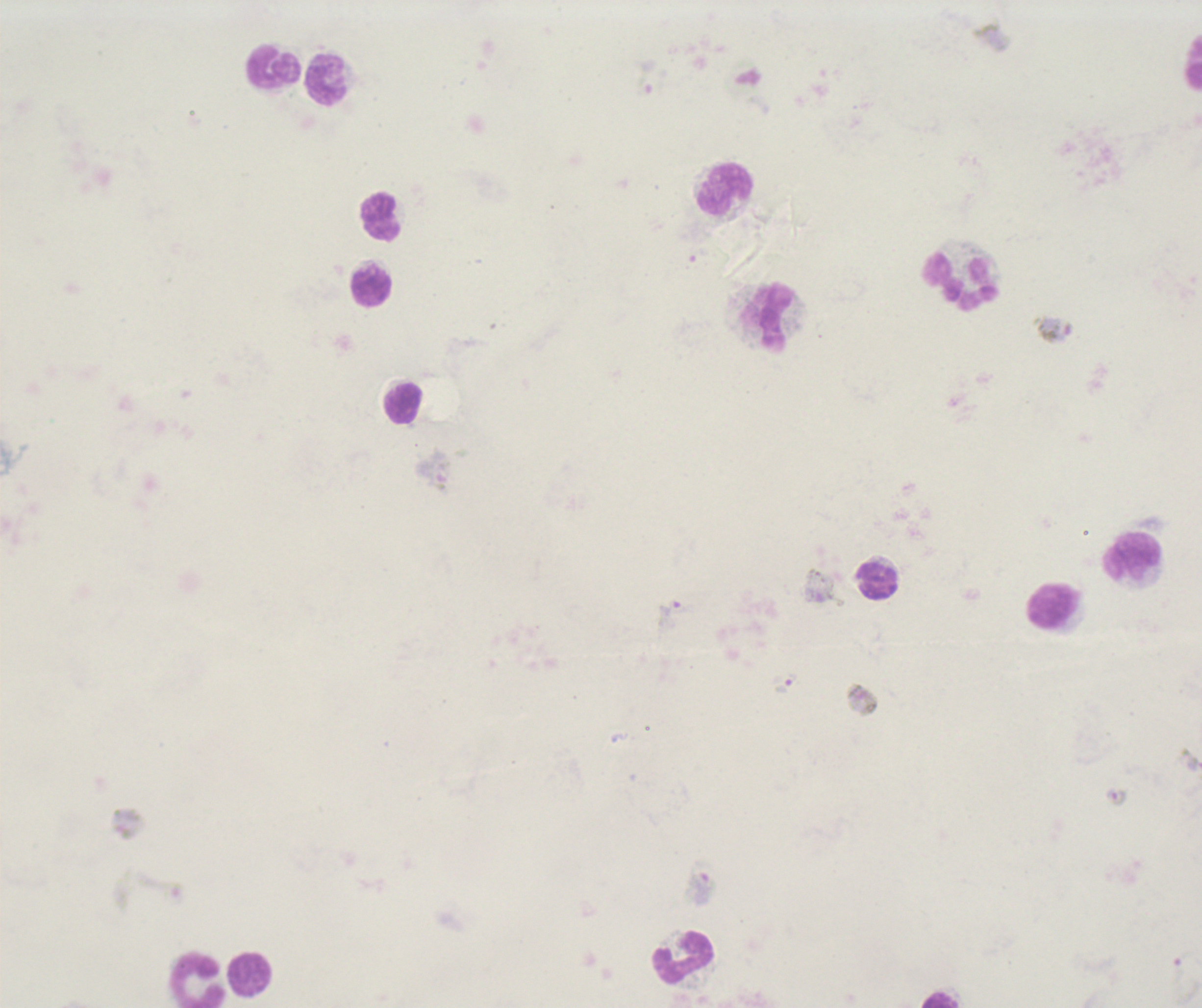

Approximate centers as [x, y] in pixels.
Summary:
  - Gametocyte locations: [435, 471], [819, 586], [668, 613], [1116, 797], [702, 887]
  - Schizont locations: [745, 78], [1053, 331]
  - Leukocyte locations: [1195, 67], [275, 69], [324, 78], [725, 190], [380, 217], [961, 281], [372, 286], [770, 318], [404, 404], [1132, 556], [875, 579], [1053, 607], [683, 958], [250, 976], [197, 980], [941, 999]
  - Life-cycle stages observed: schizont, gametocyte
  - Context: previously used in an actual diagnosis
  - Result: malaria parasites detected
  - Background quality: unsatisfactory
  - Preparation: thick blood film
  - Field of view: single
  - Image size: 1202×1008 pixels
  - Coloration quality: bad
  - Magnification: 100x
  - Stain: Romanowsky